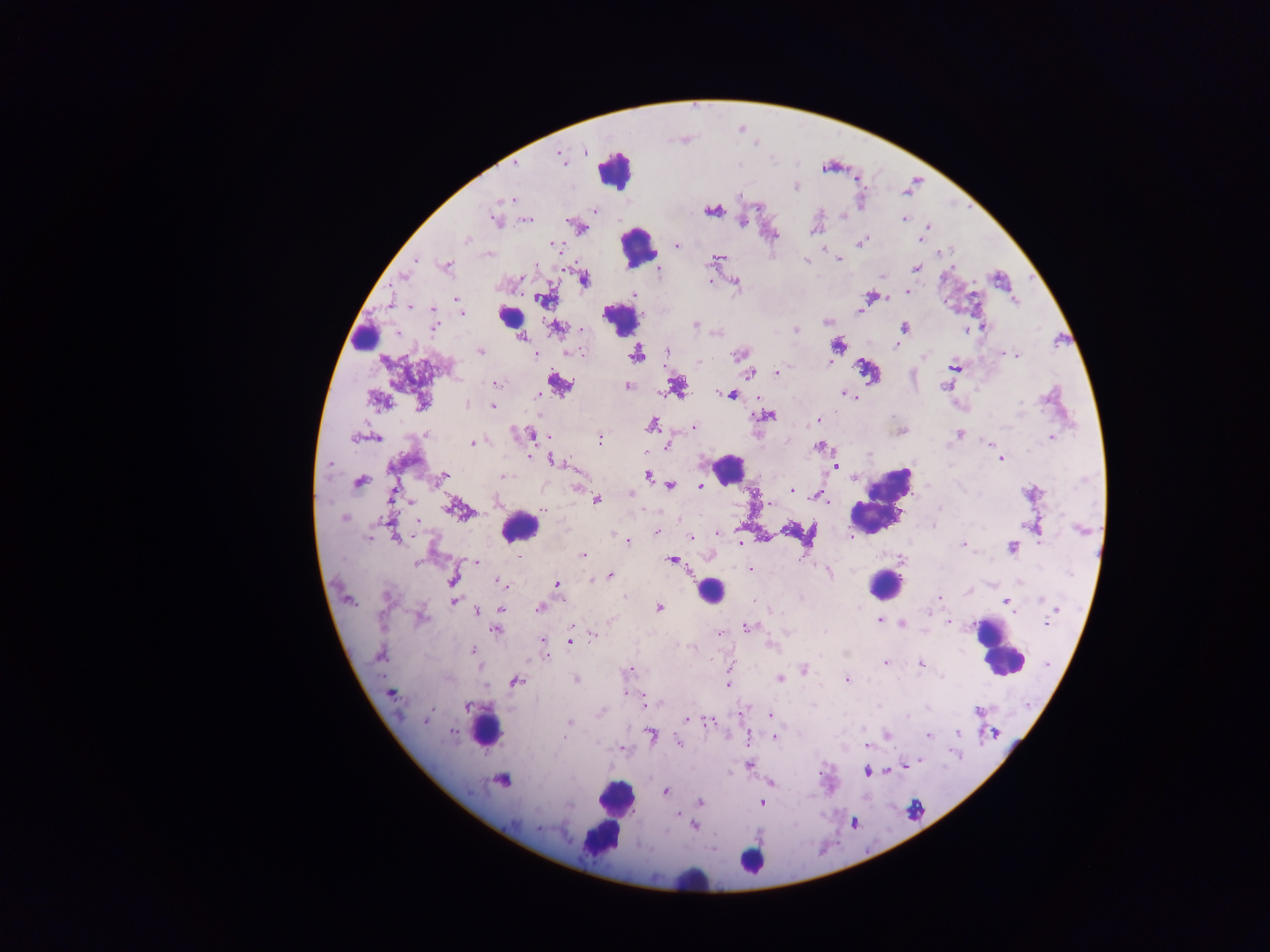

image size = 1270×952 pixels
preparation = thick blood film
country = Ghana
leukocyte locations = approximate centers as [x, y] in pixels: [616, 169], [638, 247], [512, 315], [621, 322], [359, 335], [729, 469], [883, 501], [518, 527], [885, 585], [710, 591], [997, 648], [486, 729], [504, 781], [615, 797], [599, 834], [752, 861], [697, 883]
field of view = single
capture = mobile-phone photograph through a microscope
malaria parasite locations = approximate centers as [x, y] in pixels: [585, 152], [561, 157], [515, 165], [796, 187], [511, 199], [593, 210], [712, 211], [842, 216], [904, 219], [527, 220], [495, 222], [742, 222], [928, 226], [583, 229], [814, 230], [775, 235], [467, 239], [920, 240], [863, 241], [553, 245], [677, 246], [942, 252], [715, 258], [416, 260], [839, 260], [805, 261], [447, 265], [916, 269], [659, 271], [403, 276], [882, 276], [584, 279], [710, 281], [735, 282], [908, 291], [634, 294], [870, 296], [543, 298], [457, 299], [411, 307], [859, 310], [463, 313], [827, 322], [435, 324], [695, 325], [983, 326], [556, 327], [904, 328], [582, 330], [966, 330], [796, 331], [522, 337], [839, 346], [896, 346], [481, 351], [580, 351], [666, 351], [571, 352], [637, 354], [1008, 354], [535, 355], [738, 355], [1016, 355], [923, 357], [698, 362], [830, 362], [955, 367], [777, 372], [750, 373], [495, 383], [559, 384], [627, 386], [945, 386], [678, 387], [846, 394], [731, 395], [537, 397], [379, 400], [1021, 402], [421, 403], [467, 405], [493, 406], [767, 415], [819, 420], [653, 425], [694, 427], [427, 434], [959, 434], [530, 435], [353, 437], [377, 438], [599, 438], [1051, 438], [472, 443], [987, 444], [667, 446], [819, 446], [868, 454], [531, 458], [1001, 459], [556, 462], [329, 465], [836, 465], [648, 475], [444, 476], [504, 476], [359, 482], [671, 484], [700, 485], [577, 488], [791, 490], [631, 493], [815, 495], [596, 500], [769, 503], [939, 508], [453, 509], [544, 511], [344, 518], [417, 521], [389, 523], [934, 525], [656, 532], [718, 533], [614, 535], [852, 536], [369, 538], [396, 538], [691, 538], [627, 541], [740, 543], [963, 545], [1012, 547], [584, 555], [518, 556], [901, 559], [673, 560], [417, 563], [476, 563], [749, 570], [829, 573], [610, 576], [452, 579], [592, 579], [501, 584], [557, 585], [386, 595], [624, 595], [940, 597], [1041, 599], [1005, 600], [454, 601], [658, 608], [501, 609], [539, 609], [477, 611], [1055, 611], [929, 614], [422, 618], [880, 621], [950, 622], [1046, 623], [902, 624], [747, 627], [497, 630], [720, 633], [593, 634], [544, 641], [571, 641], [772, 644], [473, 650], [546, 655], [380, 656], [885, 664], [921, 664], [803, 669], [629, 671], [780, 679], [575, 680], [847, 680], [516, 681], [728, 684], [627, 693], [391, 694], [648, 703], [467, 707], [977, 711], [601, 713], [771, 715], [908, 716], [687, 719], [426, 720], [570, 722], [709, 722], [453, 732], [958, 732], [652, 735], [886, 735], [928, 736], [774, 737], [678, 743], [866, 745], [622, 748], [914, 762], [749, 764], [866, 772], [771, 782], [665, 791], [700, 801], [762, 803], [677, 814], [694, 826], [539, 828]